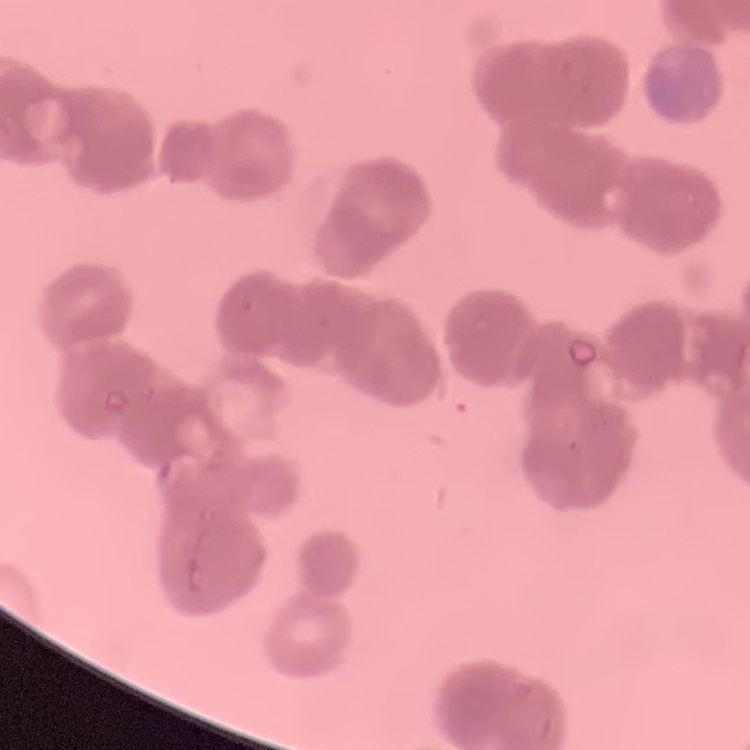

Summary:
  - Erythrocyte morphology: rouleaux formation
  - Stain: Field's or Giemsa
  - Preparation: thin blood smear
  - Image type: square crop of a larger photomicrograph